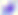

{
  "magnification": "400x",
  "identification": "Toxoplasma gondii",
  "modality": "photomicrograph"
}